Classify this cell by malaria status.
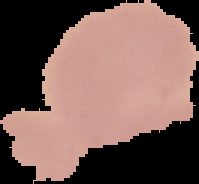

It is uninfected.

Segmented cell region on a black background. Image is 199×184 pixels. From a thin blood film.